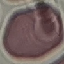

Summary:
  - Malaria status: uninfected
  - Image type: automatically extracted cell patch, resized to 64 × 64 pixels
  - Preparation: thin blood film
  - Stain: Giemsa
  - Capture: smartphone through the microscope eyepiece